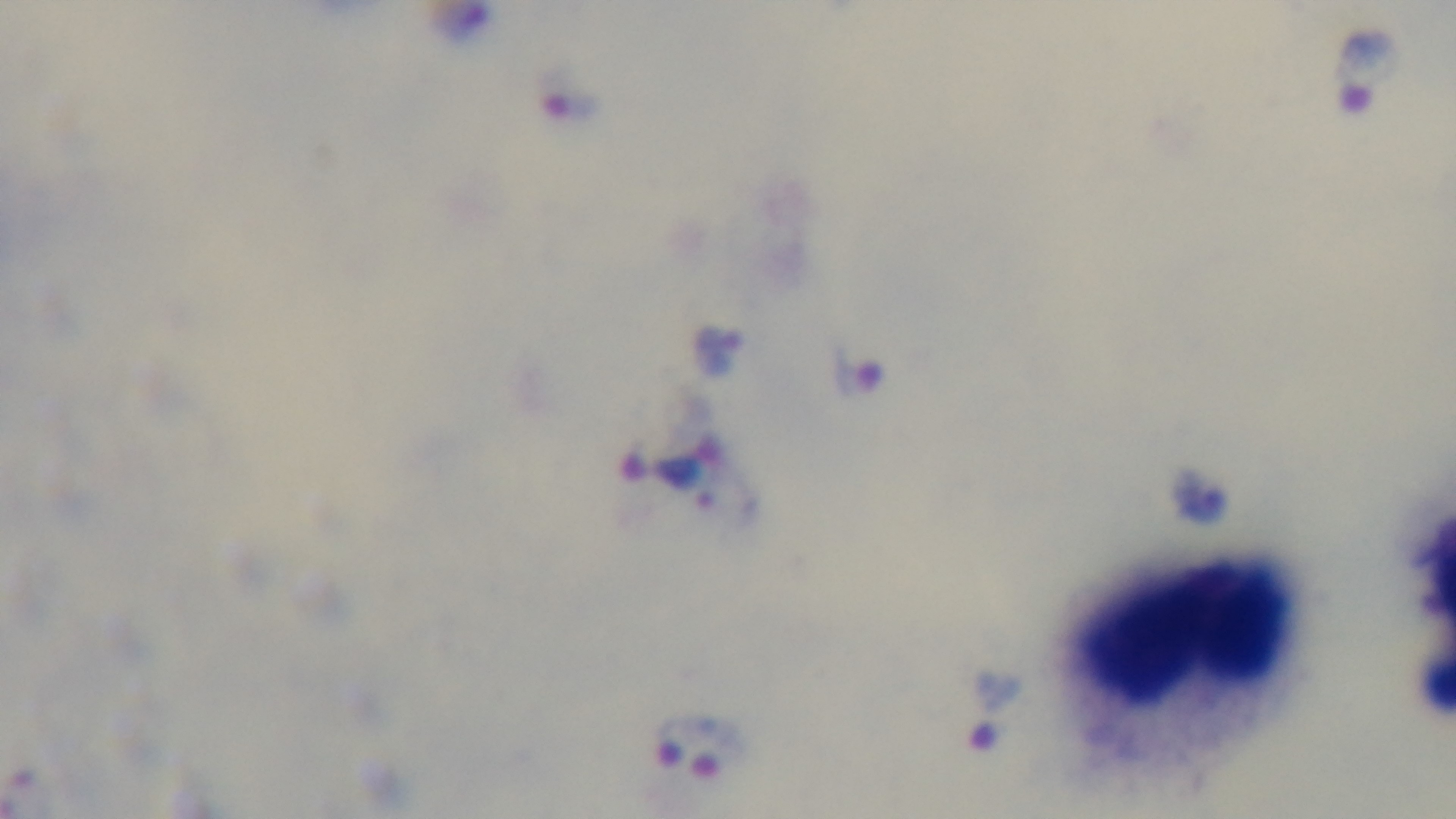
{
  "objective": "100x oil immersion",
  "modality": "light microscopy",
  "stain": "Giemsa",
  "preparation": "thick blood film",
  "malaria_status": "positive",
  "field_of_view": "single",
  "capture": "mounted 4K digital camera"
}